Locate every Plasmodium parasite.
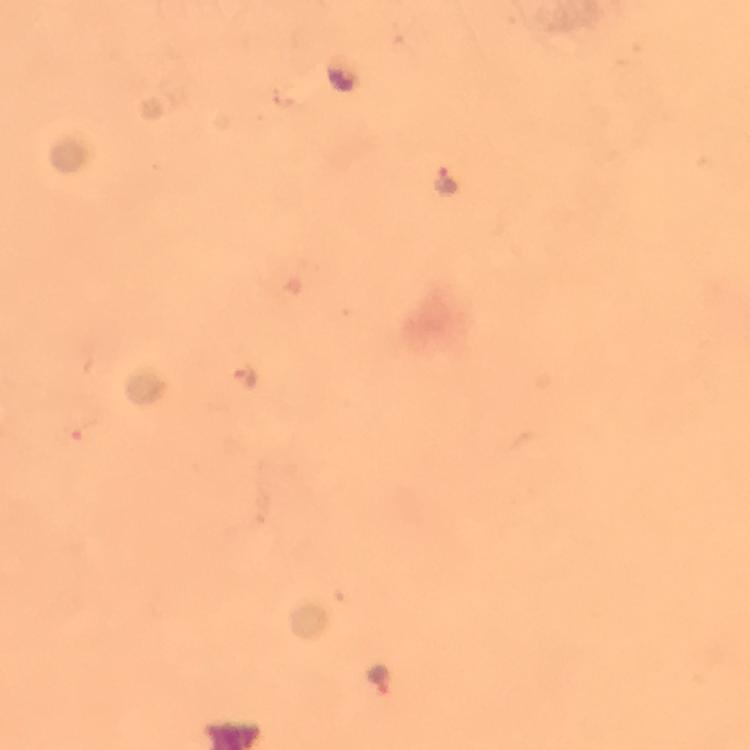
Approximate centers as (x, y) in pixels.
Plasmodium parasites: (443, 182), (246, 379), (383, 678).

Image is 750×750 pixels. Photographed with a smartphone mounted on the microscope. Immersion oil applied. A crop from one field of view. From a diagnostic examination for malaria. Giemsa stain. At 100x magnification. Thick smear.